Locate the cells, classifying each as a parasitized red blood cell, an uninfected red blood cell, or a white blood cell.
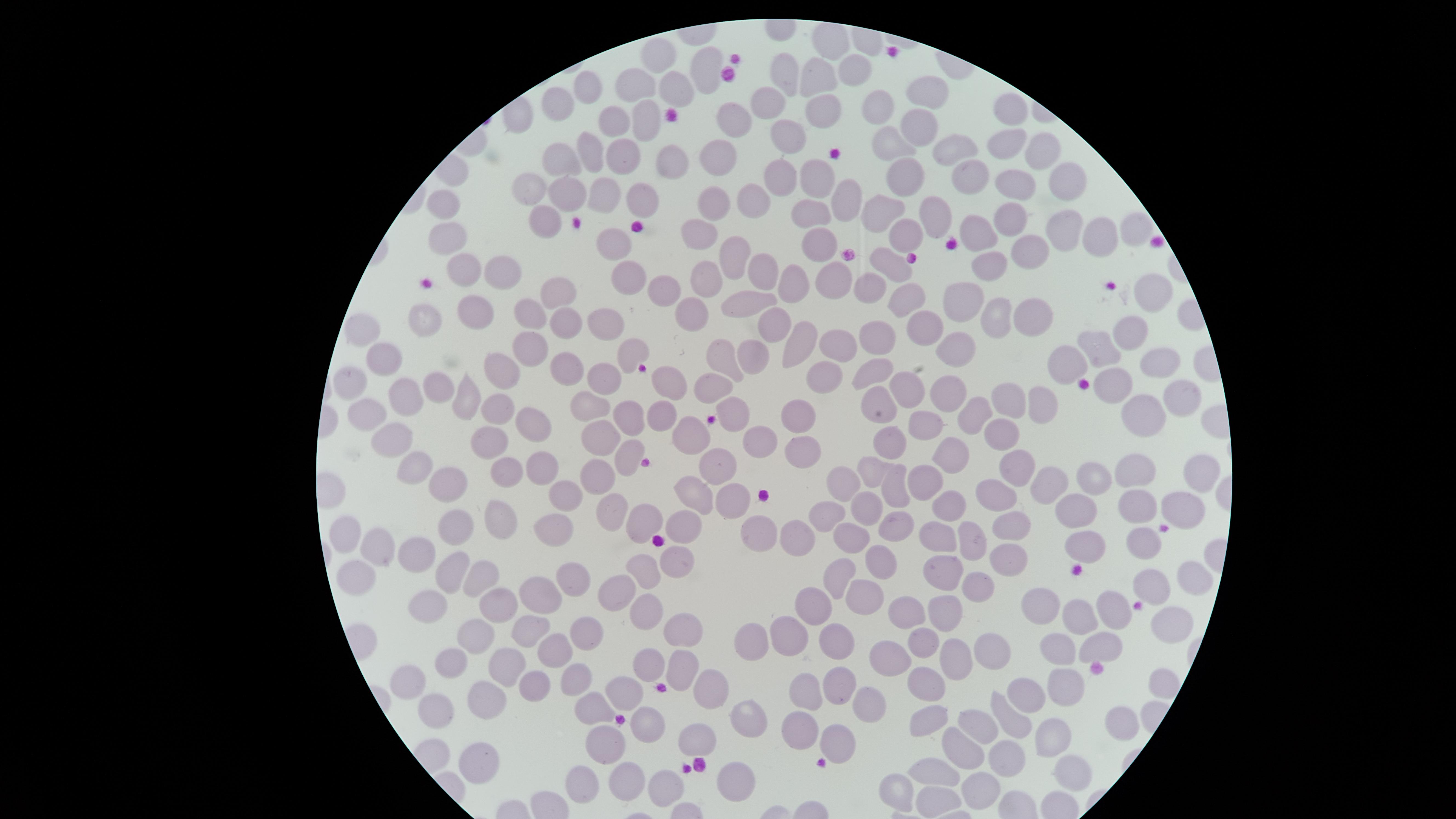
No parasitized red blood cells identified.
Approximate marker points, in pixels from the top-left corner.
Uninfected red blood cells: (x=828, y=41), (x=663, y=56), (x=701, y=70), (x=786, y=71), (x=853, y=71), (x=818, y=80), (x=635, y=84), (x=587, y=89), (x=670, y=89), (x=926, y=93), (x=559, y=101), (x=770, y=102), (x=882, y=105), (x=823, y=111), (x=1013, y=112), (x=731, y=113), (x=646, y=115), (x=609, y=122), (x=787, y=129), (x=915, y=130), (x=1007, y=144), (x=891, y=146), (x=951, y=148), (x=586, y=150), (x=1042, y=150), (x=617, y=152), (x=563, y=155), (x=716, y=156), (x=672, y=161), (x=781, y=171), (x=818, y=172), (x=906, y=173), (x=961, y=176), (x=1067, y=177), (x=531, y=182), (x=1015, y=185), (x=568, y=193), (x=602, y=193), (x=649, y=194), (x=846, y=200), (x=748, y=202), (x=444, y=203), (x=708, y=205), (x=890, y=210), (x=812, y=214), (x=935, y=214), (x=1010, y=219), (x=543, y=222), (x=1133, y=226), (x=1069, y=227), (x=906, y=232), (x=446, y=233), (x=982, y=233), (x=699, y=235), (x=614, y=239), (x=822, y=241), (x=1095, y=243), (x=1035, y=254), (x=730, y=260), (x=467, y=263), (x=892, y=265), (x=995, y=266), (x=504, y=269), (x=758, y=271), (x=835, y=277), (x=707, y=278), (x=623, y=280), (x=869, y=280), (x=790, y=283), (x=663, y=287), (x=1151, y=288), (x=558, y=290), (x=907, y=297), (x=961, y=298), (x=477, y=305), (x=746, y=306), (x=528, y=307), (x=428, y=310), (x=689, y=311), (x=1031, y=313), (x=1003, y=317), (x=610, y=322), (x=566, y=323), (x=779, y=325), (x=921, y=327), (x=1130, y=331), (x=359, y=332), (x=877, y=336), (x=802, y=341), (x=841, y=344), (x=954, y=347), (x=536, y=349), (x=1100, y=349), (x=632, y=351), (x=386, y=353), (x=755, y=354), (x=720, y=355), (x=1157, y=360), (x=1068, y=363), (x=562, y=369), (x=499, y=370), (x=877, y=374), (x=599, y=379), (x=353, y=380), (x=667, y=380), (x=827, y=381), (x=437, y=384), (x=1117, y=384), (x=907, y=386), (x=713, y=388), (x=950, y=393), (x=469, y=394), (x=401, y=396), (x=1182, y=396), (x=494, y=400), (x=878, y=400), (x=1046, y=402), (x=590, y=405), (x=734, y=405), (x=1009, y=405), (x=628, y=412), (x=368, y=414), (x=974, y=415), (x=1142, y=415), (x=798, y=418), (x=660, y=421), (x=924, y=425), (x=527, y=426), (x=998, y=432), (x=394, y=436), (x=691, y=436), (x=487, y=437), (x=596, y=442), (x=759, y=442), (x=890, y=443), (x=805, y=447), (x=951, y=448), (x=631, y=451), (x=1018, y=459), (x=408, y=465), (x=538, y=467), (x=719, y=467), (x=597, y=468), (x=511, y=469), (x=871, y=469), (x=1199, y=473), (x=1141, y=476), (x=928, y=479), (x=1092, y=480), (x=1052, y=483), (x=838, y=484), (x=449, y=488), (x=990, y=489), (x=895, y=493), (x=693, y=494), (x=562, y=497), (x=726, y=499), (x=948, y=503), (x=1181, y=504), (x=1135, y=506), (x=1076, y=509), (x=868, y=510), (x=828, y=511), (x=499, y=514), (x=614, y=514), (x=647, y=522), (x=685, y=528), (x=895, y=528), (x=1011, y=528), (x=552, y=529), (x=457, y=530), (x=794, y=532), (x=759, y=533), (x=935, y=533), (x=350, y=536), (x=852, y=537), (x=973, y=539), (x=1087, y=545), (x=1143, y=546), (x=386, y=547), (x=418, y=554), (x=998, y=557), (x=676, y=560), (x=453, y=564), (x=641, y=565), (x=883, y=565), (x=478, y=572), (x=941, y=572), (x=837, y=575), (x=356, y=577), (x=572, y=577), (x=1187, y=580), (x=1148, y=583), (x=619, y=587), (x=977, y=588), (x=540, y=597), (x=867, y=597), (x=494, y=602), (x=1046, y=602), (x=1113, y=604), (x=816, y=605), (x=906, y=607), (x=435, y=608), (x=649, y=609), (x=946, y=613), (x=1083, y=618), (x=533, y=624), (x=1168, y=624), (x=786, y=627), (x=691, y=628), (x=586, y=633), (x=479, y=635), (x=926, y=638), (x=756, y=639), (x=1107, y=639), (x=841, y=640), (x=1061, y=641), (x=554, y=649), (x=990, y=651), (x=646, y=660), (x=956, y=661), (x=509, y=662), (x=893, y=662), (x=455, y=663), (x=680, y=663), (x=580, y=676), (x=931, y=678), (x=414, y=679), (x=846, y=679), (x=1067, y=683), (x=628, y=688), (x=704, y=689), (x=808, y=690), (x=1026, y=695), (x=490, y=699), (x=864, y=702), (x=597, y=706), (x=443, y=714), (x=926, y=718), (x=749, y=720), (x=1014, y=722), (x=982, y=724), (x=646, y=725), (x=1119, y=725), (x=793, y=730), (x=1044, y=733), (x=698, y=735), (x=834, y=735), (x=611, y=744), (x=963, y=749), (x=479, y=757), (x=1005, y=762), (x=942, y=770), (x=1069, y=774), (x=582, y=777), (x=732, y=779), (x=627, y=780), (x=666, y=782), (x=976, y=789), (x=902, y=791), (x=937, y=801).
No white blood cells identified.

{
  "stain": "Giemsa",
  "capture": "smartphone photograph through the microscope eyepiece",
  "preparation": "thin blood film",
  "visible_region": "circular",
  "field_of_view": "single",
  "image_size": "1456×819 pixels"
}